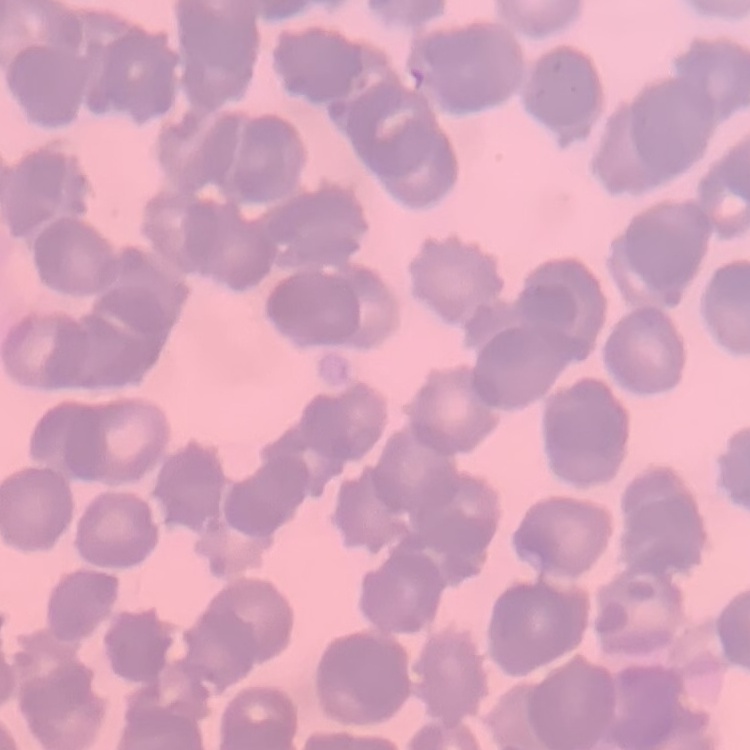
Summary:
  - Red blood cell morphology: rouleaux formation
  - Stain: Field's or Giemsa
  - Preparation: thin blood smear
  - Image type: square crop of a larger photomicrograph